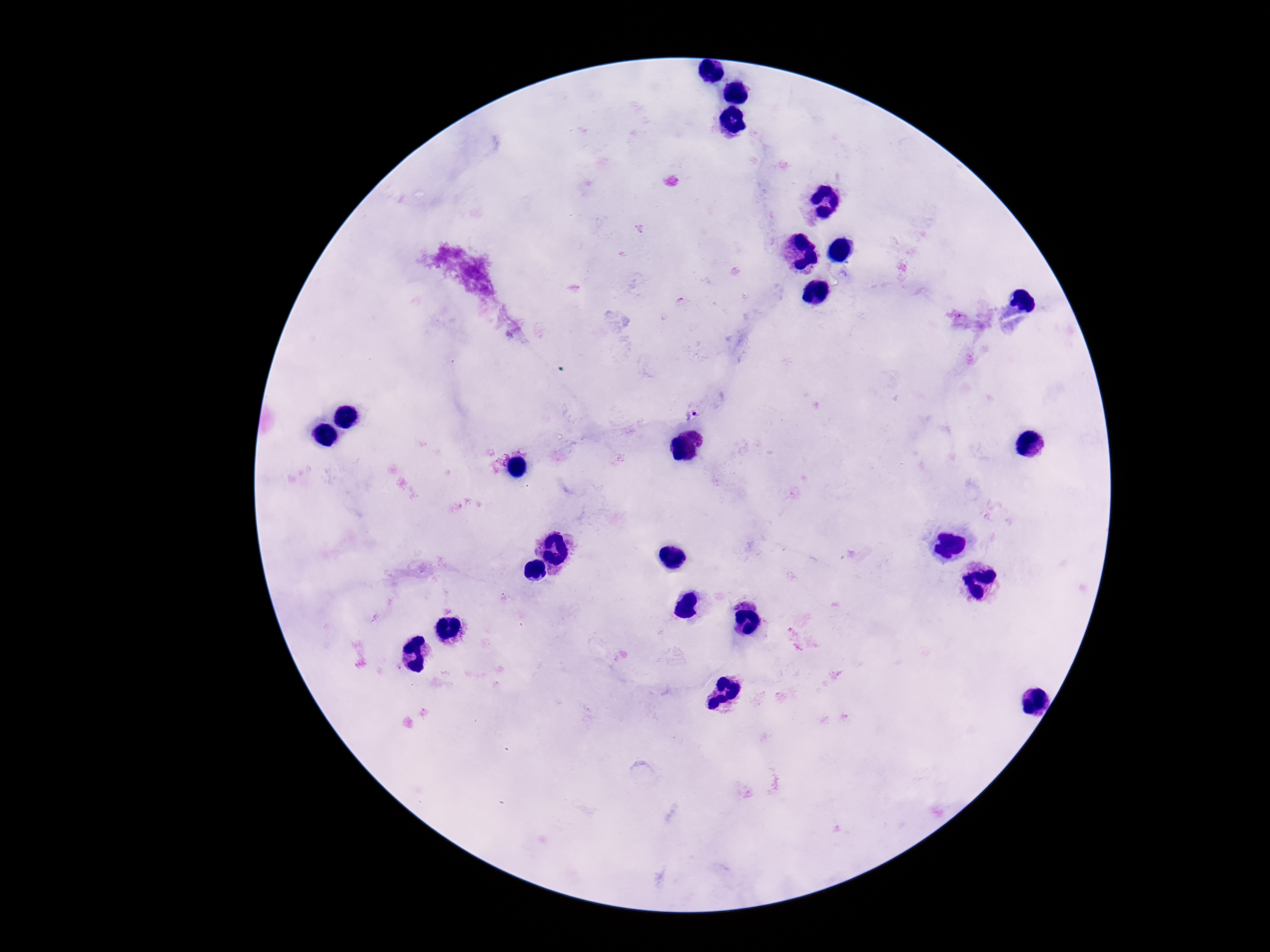

Approximate object centers, in pixels from the top-left corner.
Summary:
  - Plasmodium parasite locations: (x=691, y=415)
  - Image size: 1270×952 pixels
  - Magnification: 100x
  - Field of view: single
  - Capture: smartphone camera through the microscope eyepiece
  - Preparation: thick blood smear
  - Stain: Giemsa
  - Patient malaria status: positive